Describe the morphology of the erythrocytes.
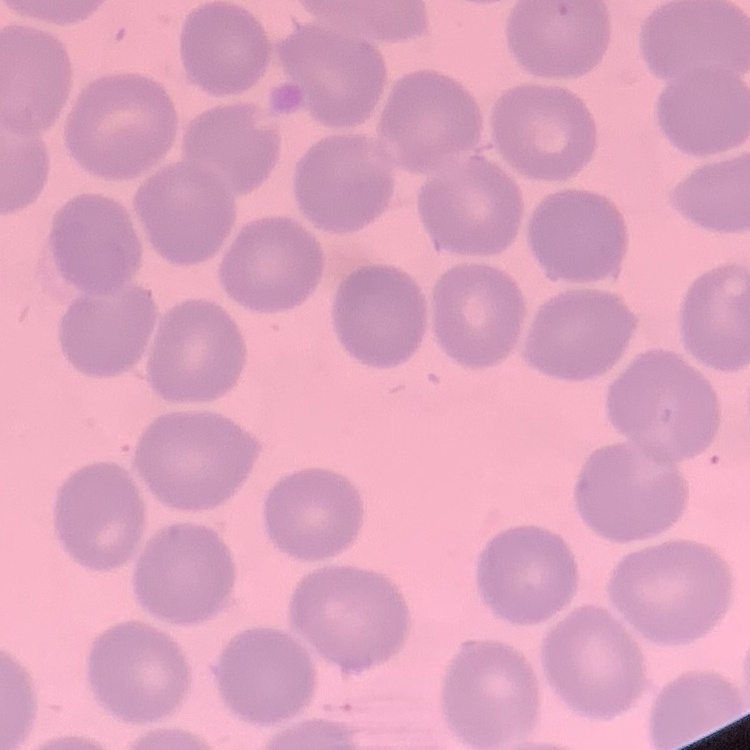

No rouleaux formation.

Summary:
  - Stain: Field's or Giemsa
  - Preparation: thin blood smear
  - Image type: square crop of a larger photomicrograph